Name the blood parasite species.
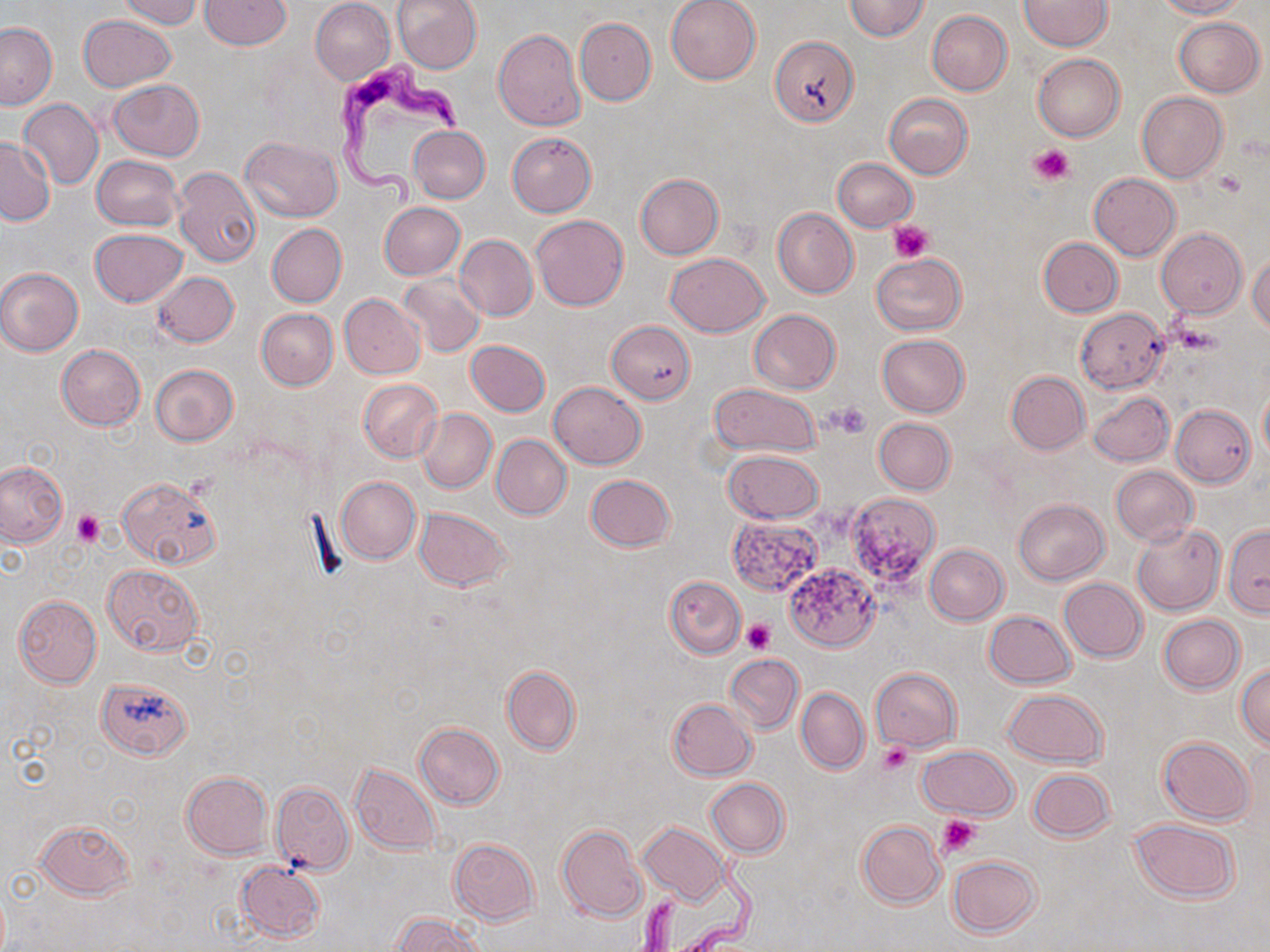
Trypanosoma brucei.

preparation: thin blood film
field_of_view: one of a larger specimen
modality: optical microscopy
uninfected_red_blood_cell_locations: 'approximate bounding boxes as named x1/y1/x2/y2 corners in pixels: (x1=117, y1=0, x2=203, y2=29), (x1=199, y1=0, x2=291, y2=51), (x1=393, y1=0, x2=482, y2=72), (x1=665, y1=0, x2=762, y2=85), (x1=844, y1=0, x2=930, y2=40), (x1=1018, y1=0, x2=1112, y2=51), (x1=1155, y1=0, x2=1246, y2=19), (x1=310, y1=1, x2=395, y2=84), (x1=926, y1=10, x2=1013, y2=95), (x1=78, y1=14, x2=177, y2=91), (x1=1173, y1=17, x2=1264, y2=97), (x1=575, y1=18, x2=655, y2=105), (x1=0, y1=23, x2=56, y2=110), (x1=494, y1=29, x2=585, y2=130), (x1=771, y1=36, x2=856, y2=125), (x1=1032, y1=53, x2=1126, y2=142), (x1=109, y1=80, x2=205, y2=160), (x1=1136, y1=91, x2=1227, y2=183), (x1=883, y1=93, x2=973, y2=178), (x1=19, y1=99, x2=104, y2=189), (x1=408, y1=125, x2=490, y2=204), (x1=507, y1=132, x2=597, y2=216), (x1=242, y1=136, x2=342, y2=222), (x1=1, y1=137, x2=55, y2=224), (x1=92, y1=155, x2=182, y2=231), (x1=832, y1=157, x2=917, y2=231), (x1=173, y1=168, x2=260, y2=267), (x1=1089, y1=173, x2=1180, y2=260), (x1=635, y1=174, x2=723, y2=259), (x1=379, y1=202, x2=465, y2=279), (x1=772, y1=207, x2=858, y2=298), (x1=531, y1=215, x2=629, y2=310), (x1=267, y1=224, x2=346, y2=307), (x1=89, y1=229, x2=188, y2=306), (x1=1156, y1=229, x2=1248, y2=318), (x1=455, y1=235, x2=538, y2=321), (x1=1038, y1=238, x2=1123, y2=317), (x1=1248, y1=252, x2=1270, y2=334), (x1=665, y1=253, x2=770, y2=337), (x1=871, y1=254, x2=966, y2=336), (x1=0, y1=268, x2=84, y2=355), (x1=153, y1=272, x2=239, y2=347), (x1=398, y1=274, x2=486, y2=358), (x1=340, y1=293, x2=424, y2=378), (x1=256, y1=308, x2=338, y2=390), (x1=1075, y1=308, x2=1169, y2=392), (x1=749, y1=309, x2=840, y2=395), (x1=609, y1=320, x2=694, y2=403), (x1=877, y1=334, x2=970, y2=417), (x1=466, y1=340, x2=550, y2=416), (x1=56, y1=345, x2=145, y2=430), (x1=151, y1=364, x2=238, y2=446), (x1=1005, y1=371, x2=1090, y2=455), (x1=359, y1=379, x2=443, y2=463), (x1=548, y1=382, x2=646, y2=468), (x1=708, y1=383, x2=821, y2=458), (x1=1259, y1=386, x2=1270, y2=464), (x1=1088, y1=391, x2=1173, y2=466), (x1=1170, y1=405, x2=1255, y2=488), (x1=416, y1=407, x2=496, y2=493), (x1=873, y1=418, x2=956, y2=495), (x1=491, y1=434, x2=572, y2=520), (x1=723, y1=450, x2=822, y2=524), (x1=0, y1=462, x2=66, y2=547), (x1=1111, y1=465, x2=1198, y2=546), (x1=585, y1=474, x2=676, y2=552), (x1=118, y1=476, x2=222, y2=567), (x1=335, y1=477, x2=420, y2=564), (x1=1014, y1=498, x2=1109, y2=584), (x1=414, y1=507, x2=511, y2=591), (x1=727, y1=518, x2=820, y2=597), (x1=1131, y1=524, x2=1225, y2=615), (x1=1223, y1=524, x2=1270, y2=613), (x1=924, y1=544, x2=1008, y2=625), (x1=787, y1=562, x2=882, y2=651), (x1=101, y1=564, x2=203, y2=656), (x1=664, y1=575, x2=747, y2=658), (x1=1059, y1=578, x2=1147, y2=662), (x1=13, y1=595, x2=103, y2=687), (x1=984, y1=610, x2=1076, y2=689), (x1=1159, y1=614, x2=1245, y2=693), (x1=725, y1=654, x2=804, y2=734), (x1=1235, y1=663, x2=1270, y2=748), (x1=501, y1=665, x2=580, y2=756), (x1=870, y1=667, x2=960, y2=752), (x1=97, y1=676, x2=193, y2=759), (x1=796, y1=688, x2=869, y2=774), (x1=1001, y1=688, x2=1108, y2=766), (x1=667, y1=699, x2=756, y2=780), (x1=414, y1=722, x2=505, y2=809), (x1=1158, y1=737, x2=1254, y2=825), (x1=918, y1=746, x2=1019, y2=818), (x1=351, y1=764, x2=441, y2=854), (x1=1027, y1=768, x2=1114, y2=842), (x1=181, y1=771, x2=271, y2=858), (x1=706, y1=779, x2=789, y2=857), (x1=270, y1=782, x2=355, y2=876), (x1=1128, y1=818, x2=1240, y2=903), (x1=34, y1=820, x2=134, y2=899), (x1=856, y1=820, x2=945, y2=908), (x1=640, y1=822, x2=730, y2=906), (x1=556, y1=824, x2=648, y2=922), (x1=448, y1=838, x2=541, y2=925), (x1=947, y1=855, x2=1041, y2=937), (x1=236, y1=861, x2=325, y2=943), (x1=393, y1=913, x2=484, y2=952)'
stain: May-Grünwald-Giemsa
platelet_locations: 'approximate bounding boxes as named x1/y1/x2/y2 corners in pixels: (x1=1030, y1=143, x2=1075, y2=186), (x1=1212, y1=169, x2=1246, y2=198), (x1=887, y1=221, x2=934, y2=264), (x1=1174, y1=321, x2=1223, y2=357), (x1=828, y1=402, x2=872, y2=438), (x1=73, y1=510, x2=106, y2=547), (x1=742, y1=618, x2=775, y2=653), (x1=878, y1=741, x2=912, y2=775), (x1=936, y1=814, x2=981, y2=857)'
trypanosoma_brucei_locations: 'approximate bounding boxes as named x1/y1/x2/y2 corners in pixels: (x1=333, y1=53, x2=470, y2=217), (x1=630, y1=842, x2=762, y2=949)'
magnification: 1000x
image_size: 1270×952 pixels